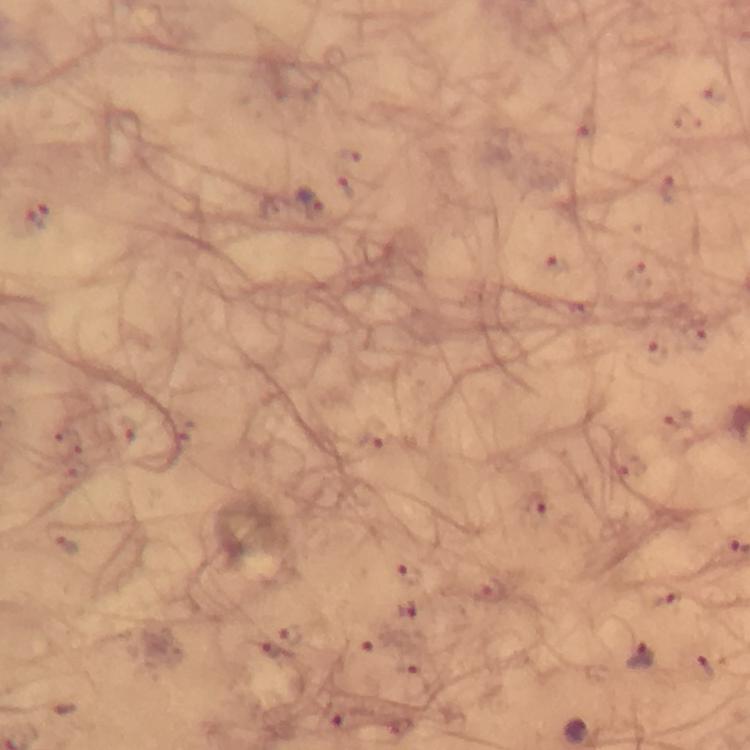
{
  "immersion_oil": "applied",
  "stain": "Giemsa",
  "cropped_from": "one field of view",
  "context": "from a malaria diagnostic workup",
  "image_size": "750×750 pixels",
  "preparation": "thick blood film",
  "plasmodium_parasite_locations": "approximate centers as (x, y) in pixels: (311, 203), (538, 505), (408, 611), (269, 648), (639, 657), (577, 731)",
  "capture": "smartphone photograph through a microscope",
  "magnification": "100x"
}